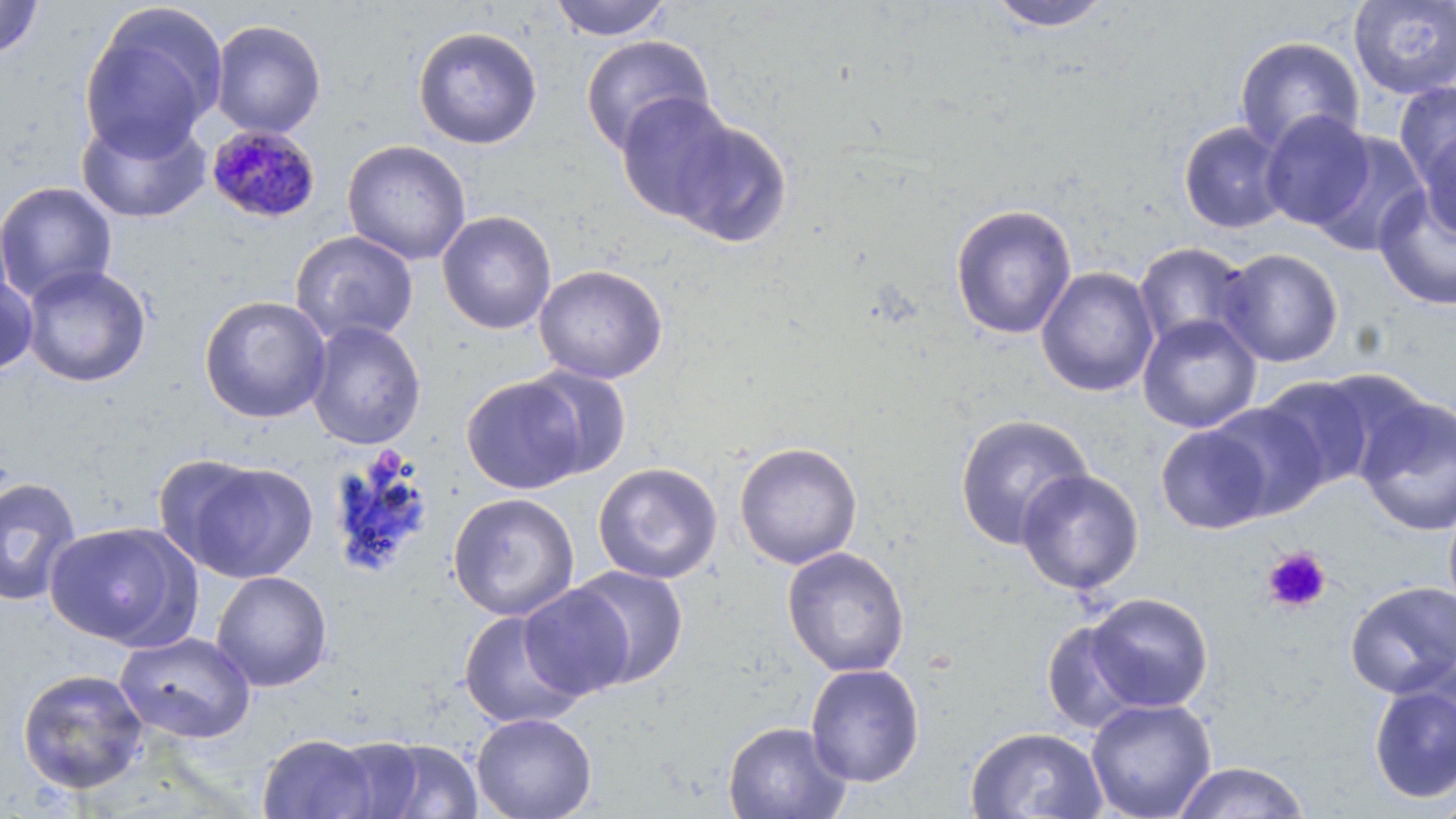

{
  "slide_level_diagnosis": "Plasmodium malariae",
  "field_of_view": "one of a larger specimen",
  "modality": "light microscopy",
  "stain": "May-Grünwald-Giemsa",
  "preparation": "thin blood film",
  "magnification": "1000x",
  "plasmodium_malariae_infected_red_blood_cell_locations": "approximate bounding boxes as [x1, y1, x2, y2] in pixels: [205, 124, 321, 225]",
  "platelet_locations": "approximate bounding boxes as [x1, y1, x2, y2] in pixels: [1261, 546, 1331, 613]",
  "uninfected_red_blood_cell_locations": "approximate bounding boxes as [x1, y1, x2, y2] in pixels: [548, 0, 674, 41], [1348, 0, 1456, 100], [0, 1, 44, 60], [984, 1, 1115, 32], [78, 3, 226, 159], [210, 19, 326, 138], [412, 25, 542, 149], [580, 35, 715, 155], [1234, 36, 1366, 154], [1393, 80, 1456, 191], [614, 91, 746, 226], [1259, 110, 1375, 231], [76, 113, 212, 224], [659, 113, 795, 248], [1179, 121, 1290, 233], [1416, 122, 1455, 242], [1308, 131, 1430, 257], [342, 140, 471, 265], [0, 182, 117, 304], [1373, 184, 1456, 311], [949, 203, 1077, 340], [437, 210, 557, 335], [290, 230, 418, 345], [1133, 241, 1255, 353], [1219, 247, 1344, 368], [20, 264, 152, 388], [533, 264, 668, 384], [1035, 266, 1159, 398], [0, 273, 39, 377], [199, 295, 332, 423], [1138, 313, 1262, 433], [305, 320, 427, 450], [522, 365, 633, 479], [1312, 368, 1432, 481], [463, 375, 588, 494], [1258, 375, 1377, 490], [1355, 395, 1456, 537], [1205, 401, 1328, 521], [954, 414, 1093, 550], [1155, 424, 1273, 534], [734, 441, 863, 569], [173, 459, 318, 583], [592, 462, 723, 584], [1016, 468, 1145, 595], [0, 476, 83, 607], [447, 492, 579, 621], [1443, 498, 1456, 621], [45, 521, 198, 651], [782, 546, 910, 677], [567, 566, 689, 688], [210, 570, 333, 692], [1345, 580, 1456, 698], [517, 583, 636, 701], [1084, 592, 1212, 712], [458, 609, 587, 730], [1040, 618, 1147, 733], [114, 631, 256, 744], [805, 663, 925, 787], [16, 668, 149, 795], [1367, 675, 1456, 806], [1085, 698, 1217, 819], [471, 712, 597, 819], [723, 721, 852, 819], [965, 726, 1107, 818], [257, 733, 380, 818], [324, 736, 430, 818], [367, 738, 484, 819], [1170, 761, 1312, 819], [1427, 789, 1456, 819]",
  "image_size": "1456×819 pixels"
}